Identify the parasite.
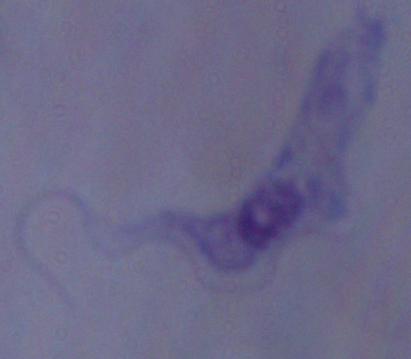

A trypanosome.

magnification: 1000x
modality: photomicrograph